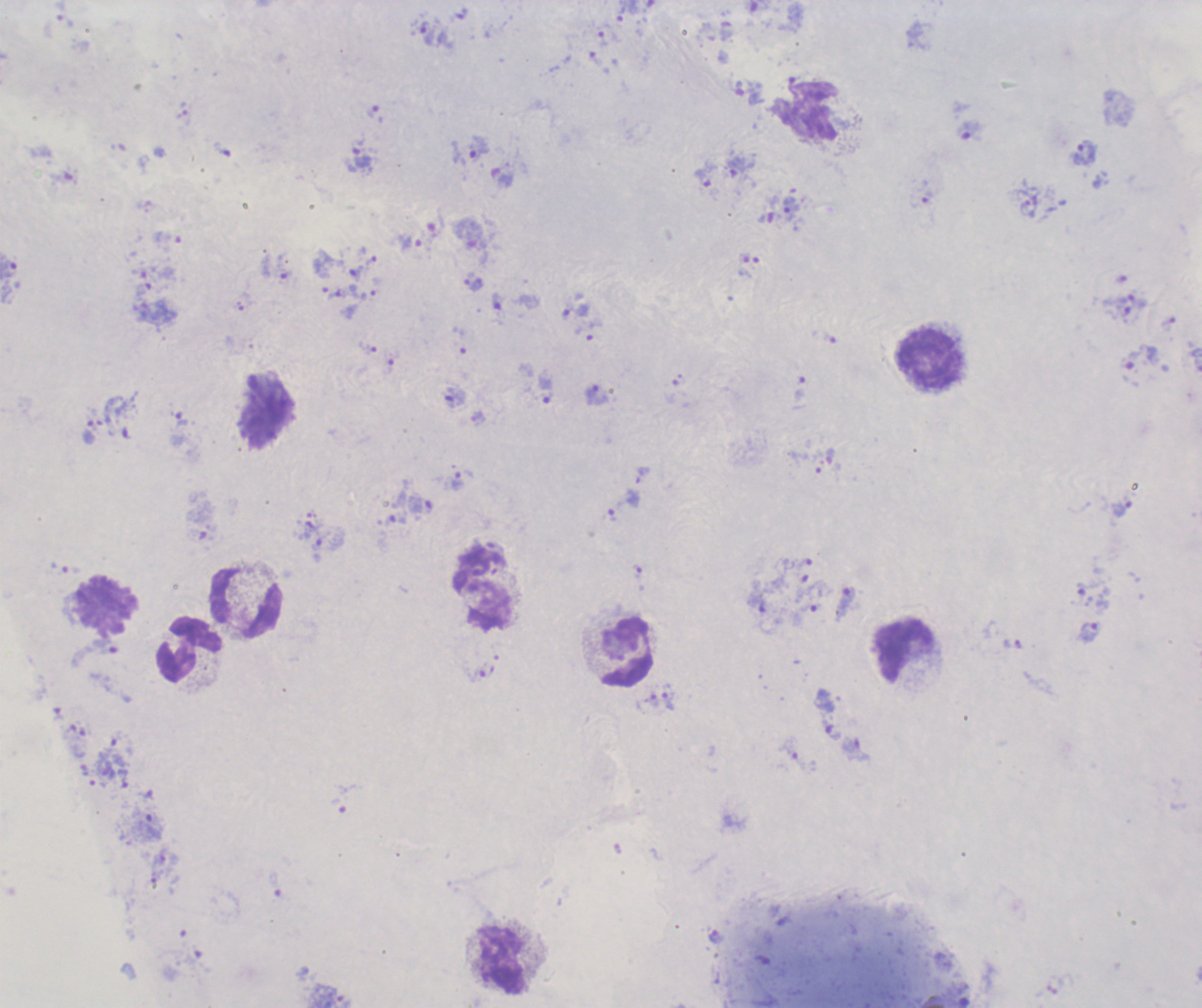 Approximate centers as (x, y) in pixels. Leukocyte locations: (806, 111), (930, 359), (484, 588), (247, 601), (107, 604), (189, 649), (904, 651), (626, 652), (502, 960). Trophozoite locations: (427, 34), (603, 39), (478, 148), (1085, 154), (360, 160), (736, 166), (703, 179), (791, 208), (411, 244), (357, 273), (474, 282), (496, 302), (576, 311), (546, 389), (597, 395), (455, 396), (181, 420), (89, 432), (458, 481), (1122, 508), (305, 529), (637, 571), (844, 603), (1089, 631), (655, 700), (668, 701), (716, 937). Previously used in a real diagnosis. Single field of view. Result: malaria parasites detected. Image is 1202×1008 pixels. Thick blood film. Captured at 100x magnification. Background quality: poor. Romanowsky stain.